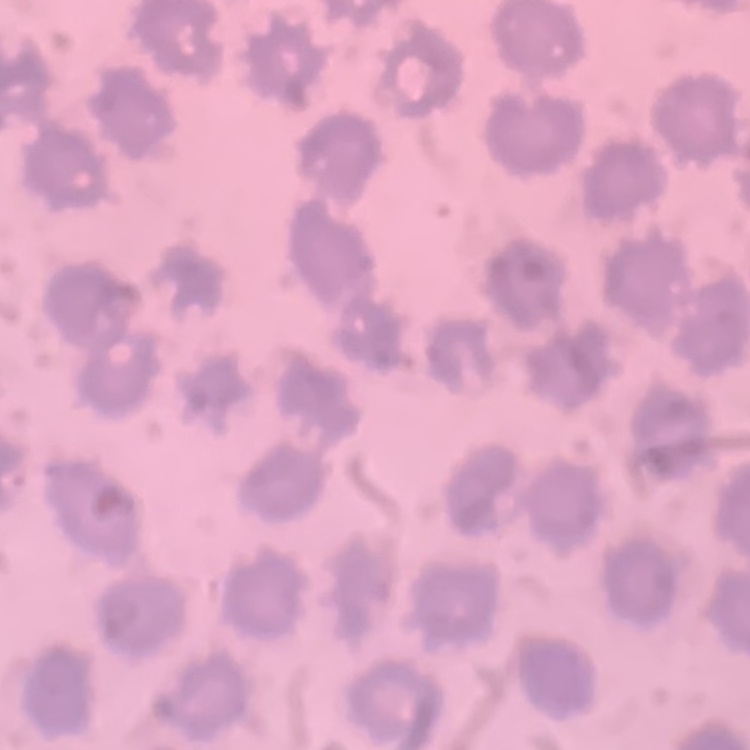
Summary:
  - Erythrocyte morphology: no rouleaux formation
  - Image type: square crop of a larger photomicrograph
  - Preparation: thin blood film
  - Stain: Field's or Giemsa